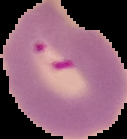
image_size: 127×139 pixels
result: malaria parasites detected
preparation: thin blood film
image_type: cell region segmented out of the field of view; surrounding area masked to black